Locate every blood parasite and identify its species.
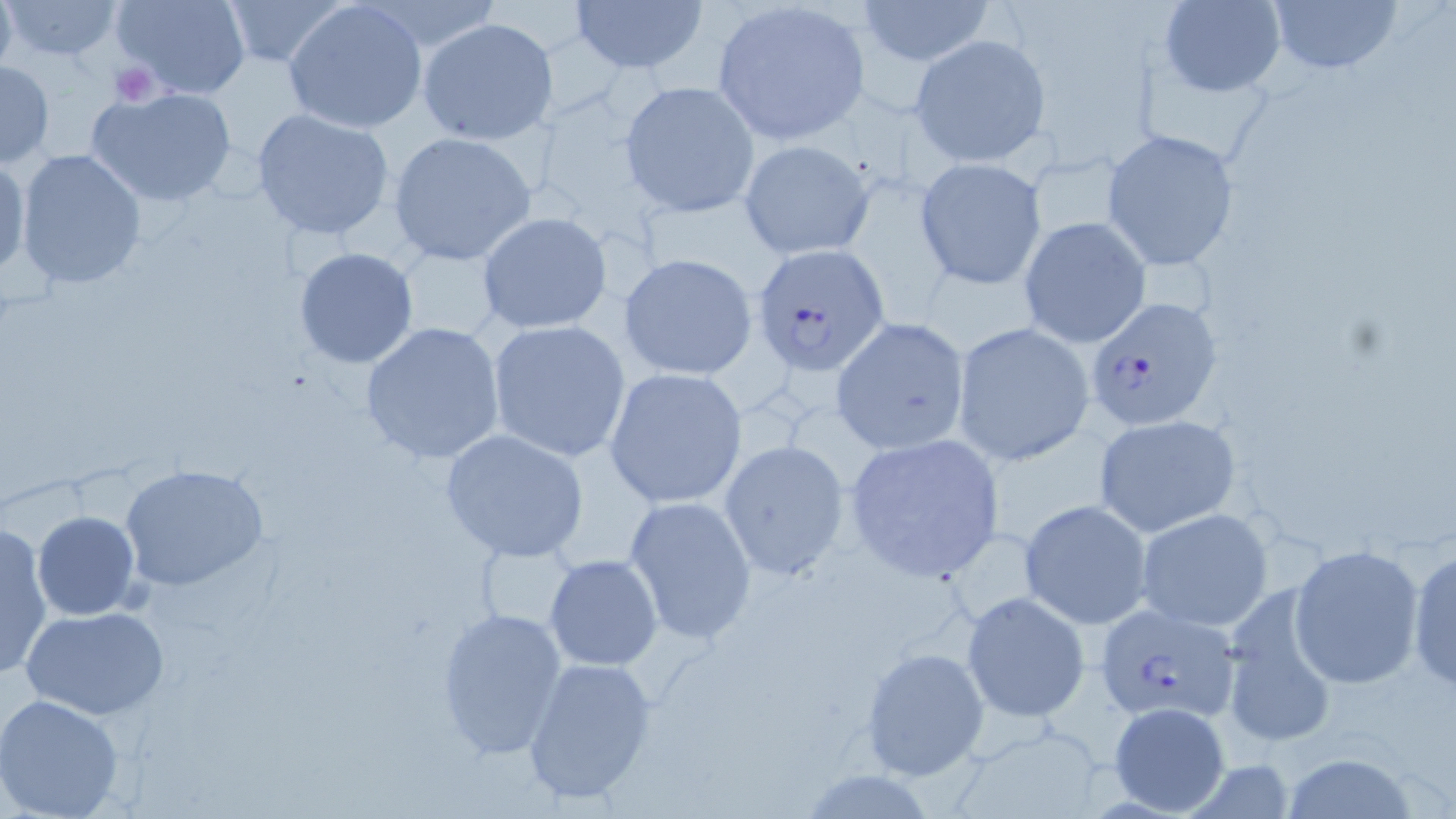

Approximate bounding boxes as (x1,y1)-(x2,y2) corner pairs in pixels.
Plasmodium falciparum-infected red blood cells: (750,242)-(889,374), (1085,296)-(1224,432), (1095,601)-(1240,723).
No Plasmodium ovale, Plasmodium malariae, Plasmodium vivax, Babesia divergens, or Trypanosoma brucei observed.

slide-level diagnosis = Plasmodium falciparum
field of view = single
magnification = 1000x
stain = May-Grünwald-Giemsa
modality = light microscopy
preparation = thin blood smear
image size = 1456×819 pixels
platelet locations = approximate bounding boxes as (x1,y1)-(x2,y2) corner pairs in pixels: (108,61)-(160,106)
uninfected red blood cell locations = approximate bounding boxes as (x1,y1)-(x2,y2) corner pairs in pixels: (0,0)-(18,77), (109,0)-(251,100), (218,0)-(350,66), (568,0)-(710,77), (1157,0)-(1286,96), (1267,0)-(1401,77), (1,1)-(127,62), (282,1)-(427,134), (856,1)-(994,63), (710,4)-(873,144), (417,18)-(559,144), (909,33)-(1053,169), (0,59)-(54,167), (619,82)-(761,216), (85,87)-(239,208), (250,109)-(397,243), (1101,128)-(1241,270), (388,132)-(536,266), (737,138)-(876,260), (14,148)-(148,289), (0,155)-(30,279), (914,157)-(1048,289), (477,212)-(615,335), (1017,217)-(1150,349), (294,247)-(419,368), (618,253)-(758,381), (830,317)-(969,455), (486,320)-(631,462), (358,322)-(507,465), (952,322)-(1095,467), (604,367)-(749,509), (1093,413)-(1241,536), (439,428)-(590,562), (1113,429)-(1260,616), (841,433)-(1006,584), (717,440)-(850,581), (119,463)-(270,593), (623,495)-(758,645), (1018,499)-(1152,629), (1136,508)-(1274,633), (33,511)-(140,620), (0,522)-(52,679), (1289,544)-(1425,689), (1406,544)-(1455,693), (544,555)-(663,671), (1220,590)-(1341,748), (961,591)-(1090,722), (22,605)-(170,719), (434,605)-(568,761), (860,648)-(990,782), (521,655)-(660,807), (0,694)-(126,819), (1107,702)-(1232,815), (1278,751)-(1421,819)